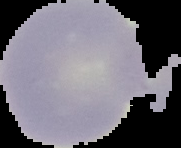

image_size: 181×148 pixels
image_type: segmented cell region on a black background
malaria_status: uninfected
preparation: thin blood film